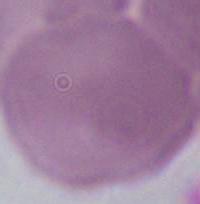
{
  "identification": "red blood cell",
  "magnification": "1000x",
  "modality": "photomicrograph"
}